State the blood parasite species.
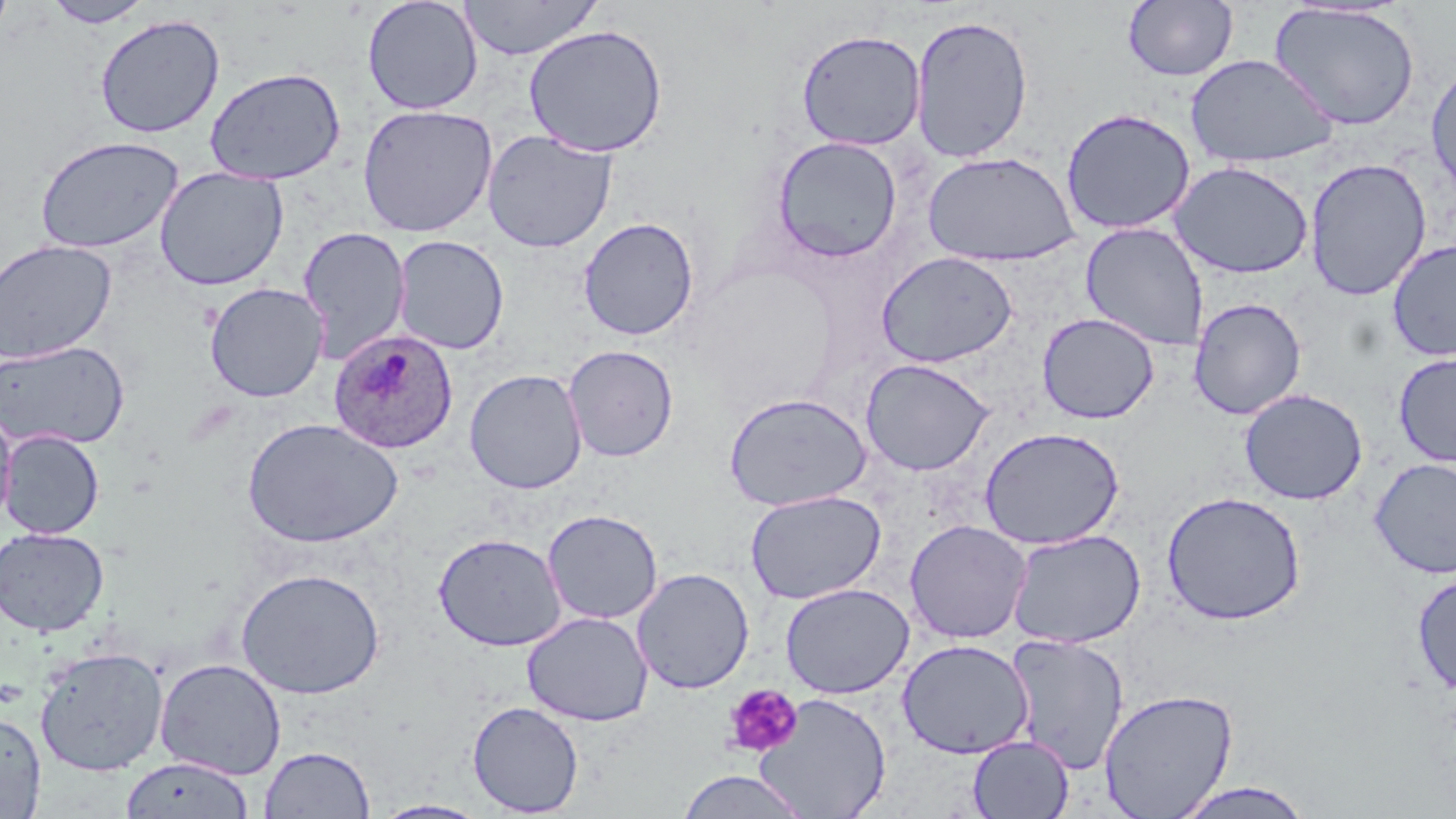
Plasmodium ovale.

modality = optical microscopy
stain = May-Grünwald-Giemsa
field of view = single
image size = 1456×819 pixels
uninfected red blood cell locations (subset) = approximate bounding boxes as (x1,y1)-(x2,y2) corner pairs in pixels: (362,0)-(484,115), (457,0)-(602,61), (0,1)-(15,44), (44,1)-(153,28), (1123,1)-(1238,82), (1269,3)-(1421,131), (94,13)-(225,138), (909,14)-(1034,163), (523,24)-(668,158), (795,29)-(926,151), (1185,54)-(1337,169), (1426,60)-(1456,202), (204,67)-(346,185), (357,104)-(498,237), (1060,107)-(1196,235), (482,129)-(617,253), (34,135)-(184,254), (772,136)-(903,263), (922,151)-(1079,267), (1304,158)-(1432,301), (1169,161)-(1314,279), (154,166)-(289,291), (577,216)-(700,341), (1080,222)-(1210,352), (298,227)-(411,363), (392,235)-(509,354), (0,239)-(117,364), (1386,239)-(1456,362), (875,251)-(1018,367), (1189,297)-(1306,420), (1037,312)-(1160,424), (0,339)-(129,451), (563,344)-(679,462), (1393,352)-(1456,468), (859,358)-(995,476), (464,368)-(587,494), (1239,388)-(1368,505), (723,392)-(872,511), (0,403)-(17,530), (242,418)-(404,549), (979,426)-(1125,550), (1,429)-(104,540), (1369,458)-(1456,579), (744,490)-(885,604), (1162,491)-(1307,626), (542,509)-(663,625), (904,519)-(1032,643), (0,527)-(109,637), (1007,529)-(1145,648), (433,532)-(567,651), (631,567)-(755,694), (235,568)-(385,699), (1412,572)-(1456,697), (781,583)-(913,698), (521,611)-(654,726), (1005,633)-(1129,774), (896,639)-(1034,759), (34,646)-(168,776), (155,658)-(287,780), (1099,687)-(1238,819), (755,693)-(892,818), (467,701)-(584,817), (0,708)-(47,818), (967,735)-(1074,818), (259,745)-(375,818), (120,756)-(254,818), (674,770)-(812,818), (1168,781)-(1319,818), (371,799)-(491,818)
platelet locations = approximate bounding boxes as (x1,y1)-(x2,y2) corner pairs in pixels: (722,683)-(802,757)
preparation = thin blood smear
magnification = 1000x
Plasmodium ovale-infected red blood cell locations (subset) = approximate bounding boxes as (x1,y1)-(x2,y2) corner pairs in pixels: (328,328)-(458,454)